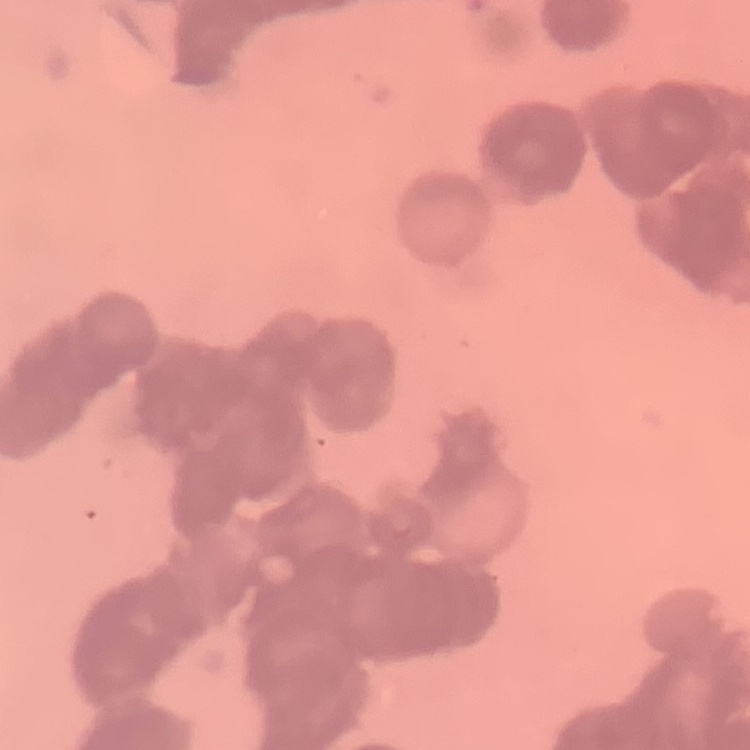 The red blood cells exhibit rouleaux formation. Field's or Giemsa stain. One tile cut from a larger photomicrograph. Thin peripheral smear.